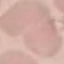
{
  "result": "no malaria parasites seen",
  "capture": "smartphone through the microscope eyepiece",
  "image_type": "automatically extracted cell patch, resized to 64 × 64 pixels",
  "preparation": "thin blood smear",
  "stain": "Giemsa"
}